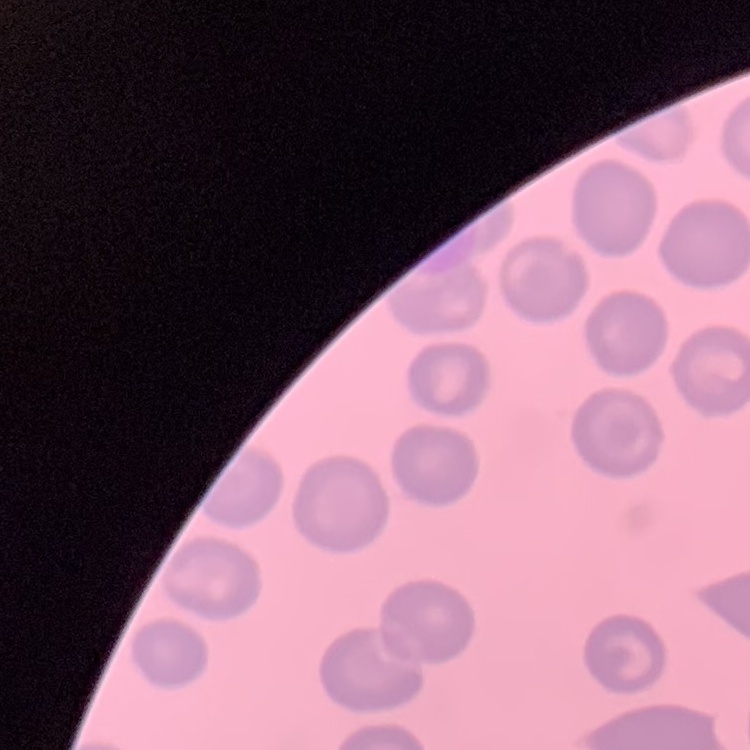

red blood cell morphology = no rouleaux formation
stain = Field's or Giemsa
preparation = thin peripheral smear
image type = square crop of a larger photomicrograph